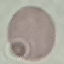

Summary:
  - Malaria status: uninfected
  - Preparation: thin blood smear
  - Stain: Giemsa
  - Capture: smartphone through the microscope eyepiece
  - Image type: cell patch, automatically extracted from a larger field of view and resized to 64 × 64 pixels